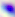 Toxoplasma gondii is shown. Photomicrograph. Captured at 400x magnification.